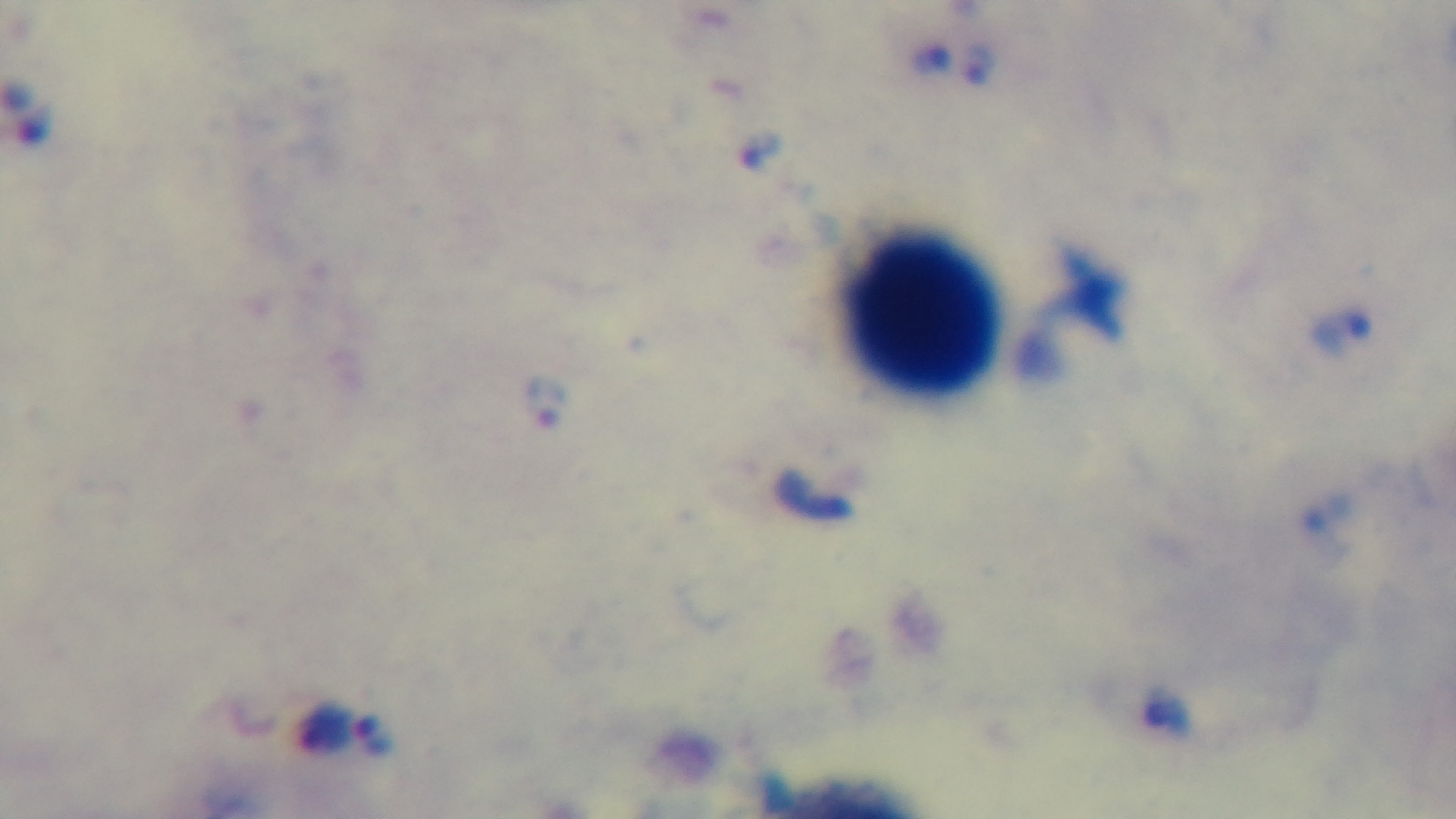

Summary:
  - Objective: 100x oil immersion
  - Capture: mounted 4K digital camera
  - Stain: Giemsa
  - Preparation: thick smear
  - Field of view: single
  - Modality: light microscopy
  - Malaria status: positive